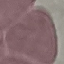
Summary:
  - Result: negative for malaria parasites
  - Capture: smartphone through the microscope eyepiece
  - Stain: Giemsa
  - Image type: automatically extracted cell patch, resized to 64 × 64 pixels
  - Preparation: thin blood smear